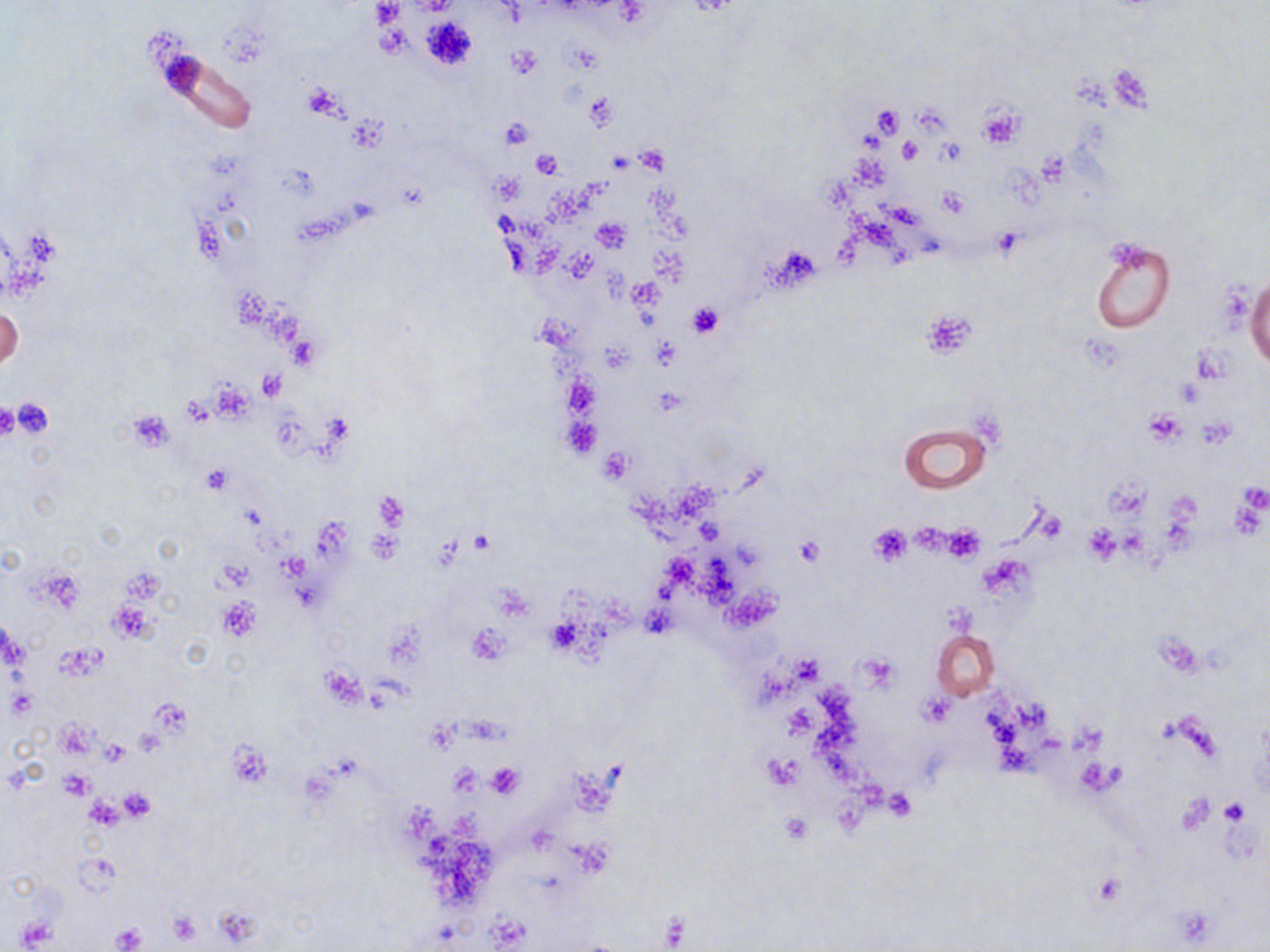
slide-level diagnosis = no evidence of blood parasites
platelet locations = approximate bounding boxes as (x1, y1, x2, y2) in pixels: (373, 2, 402, 27), (421, 16, 478, 71), (507, 47, 542, 78), (302, 83, 348, 118), (585, 94, 618, 130), (976, 102, 1026, 149), (872, 107, 903, 137), (349, 118, 388, 149), (500, 118, 534, 149), (898, 139, 922, 163), (936, 141, 966, 167), (637, 145, 669, 174), (531, 149, 565, 178), (938, 188, 969, 217), (593, 216, 630, 252), (991, 228, 1024, 256), (770, 245, 822, 289), (687, 302, 723, 338), (923, 310, 973, 356), (258, 368, 288, 400), (1174, 380, 1205, 408), (652, 387, 686, 416), (10, 398, 55, 441), (0, 403, 20, 441), (1143, 411, 1184, 445), (127, 412, 174, 450), (599, 447, 633, 482), (202, 465, 233, 493), (1104, 472, 1149, 521), (1236, 483, 1269, 513), (373, 492, 408, 533), (868, 523, 911, 567), (942, 524, 985, 562), (1082, 525, 1121, 564), (367, 529, 402, 563), (794, 537, 823, 567), (216, 597, 260, 641), (545, 615, 583, 655), (466, 624, 511, 665), (320, 666, 366, 708), (918, 693, 959, 729), (100, 738, 129, 764), (225, 739, 273, 788), (763, 752, 804, 790), (1077, 759, 1123, 795), (485, 763, 524, 799), (448, 765, 482, 800), (58, 770, 96, 799), (119, 787, 157, 823), (883, 789, 916, 822), (1179, 793, 1216, 834), (84, 797, 124, 830), (1219, 799, 1251, 826), (780, 812, 814, 844), (166, 911, 203, 945), (15, 917, 55, 948), (111, 923, 147, 952)
uninfected red blood cell locations = approximate bounding boxes as (x1, y1, x2, y2) in pixels: (1091, 240, 1175, 333), (1246, 274, 1269, 373), (1, 306, 23, 372), (900, 423, 990, 493), (931, 629, 999, 698)
modality = light microscopy
magnification = 1000x
preparation = thin blood smear
field of view = single
image size = 1270×952 pixels
stain = May-Grünwald-Giemsa